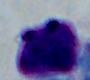

modality = photomicrograph
identification = leukocyte
magnification = 1000x